State which parasite is depicted.
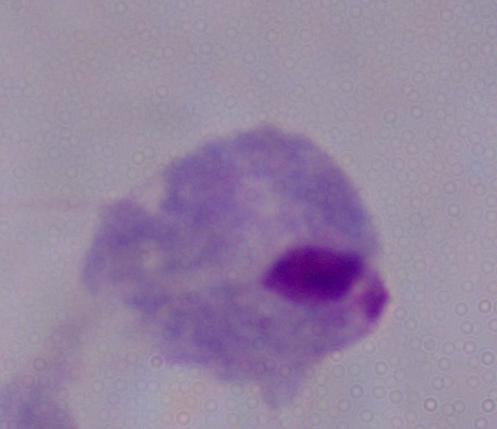

This is a trichomonad.

Micrograph. 1000x magnification.